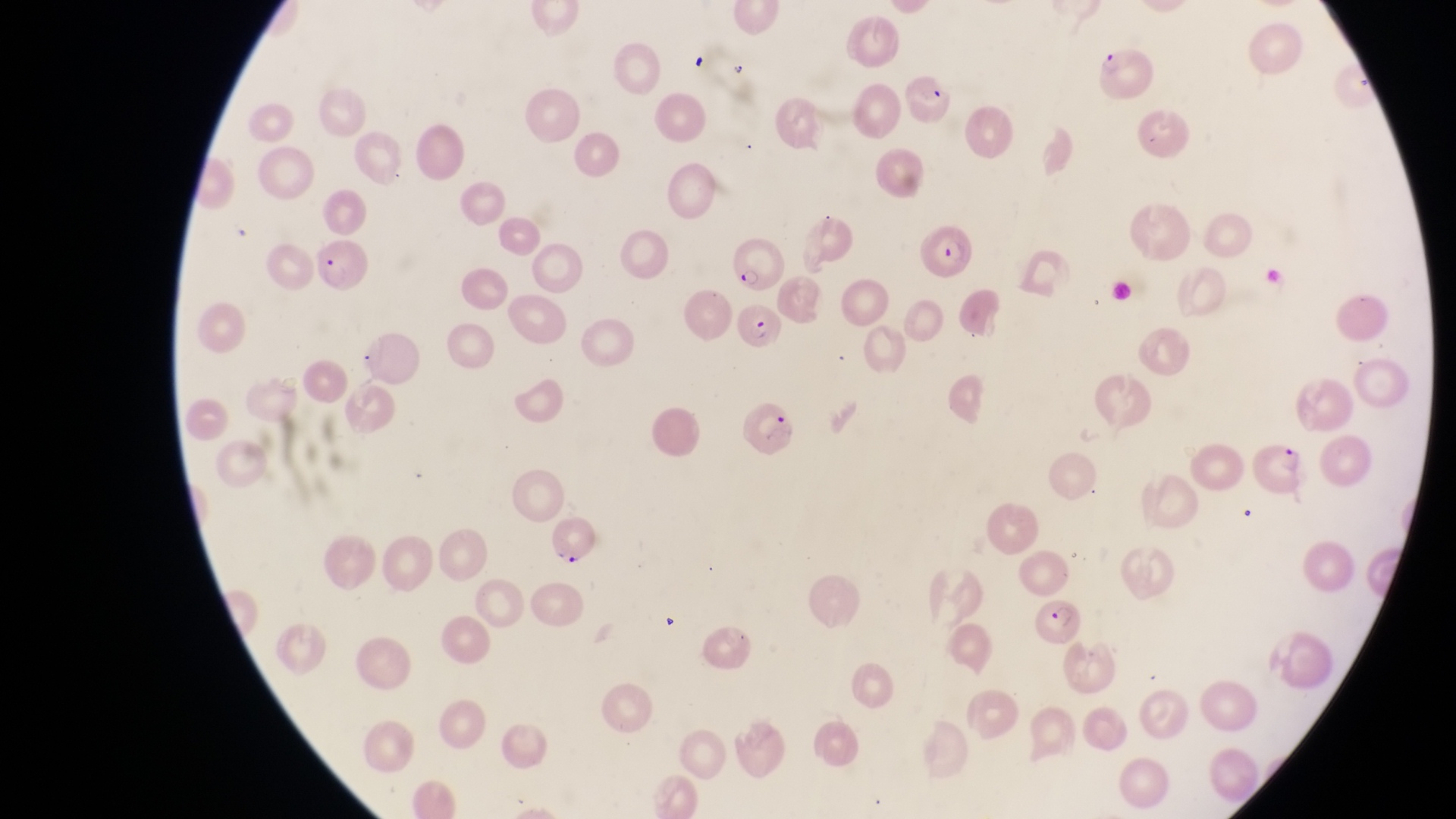
Approximate bounding boxes as [left, top, right, bottom] in pixels. Parasitised red blood cell locations: [1100, 44, 1158, 102], [920, 227, 978, 282], [314, 240, 367, 293], [740, 297, 786, 355], [748, 400, 795, 458], [1257, 442, 1309, 501], [547, 512, 602, 565], [1037, 597, 1086, 646]. Magnification of 1000x. Collected in Uganda. Thin blood smear. Image is 1456×819 pixels. Captured by a smartphone held over the eyepiece of an Olympus CX-23 microscope. One field of view.